Assess the morphology of the red blood cells.
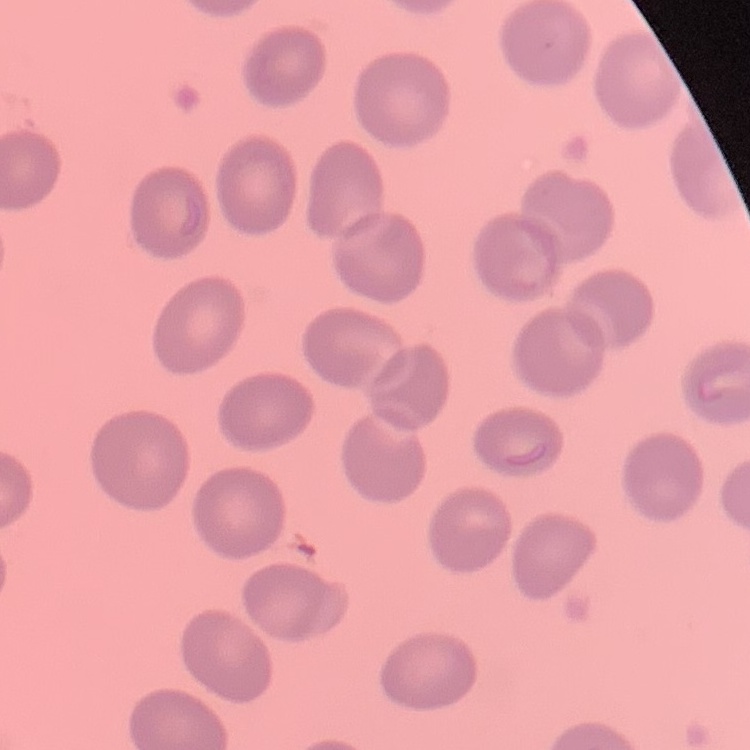

They show no rouleaux formation.

preparation = thin blood film
stain = Field's or Giemsa
image type = one tile cut from a larger photomicrograph